Assess this cell for malaria.
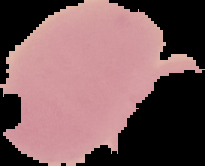
It is uninfected.

Summary:
  - Image size: 205×166 pixels
  - Preparation: thin blood film
  - Image type: segmented cell region on a black background